State which parasite is depicted.
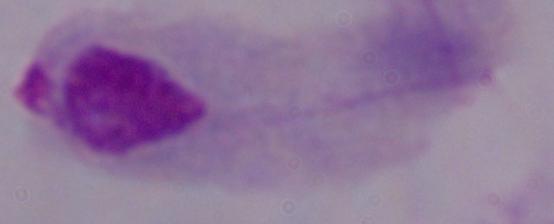
A trichomonad.

modality = photomicrograph
magnification = 1000x